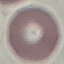

Summary:
  - Malaria status: uninfected
  - Image type: automatically extracted cell patch, resized to 64 × 64 pixels
  - Preparation: thin smear
  - Capture: smartphone through the microscope eyepiece
  - Stain: Giemsa